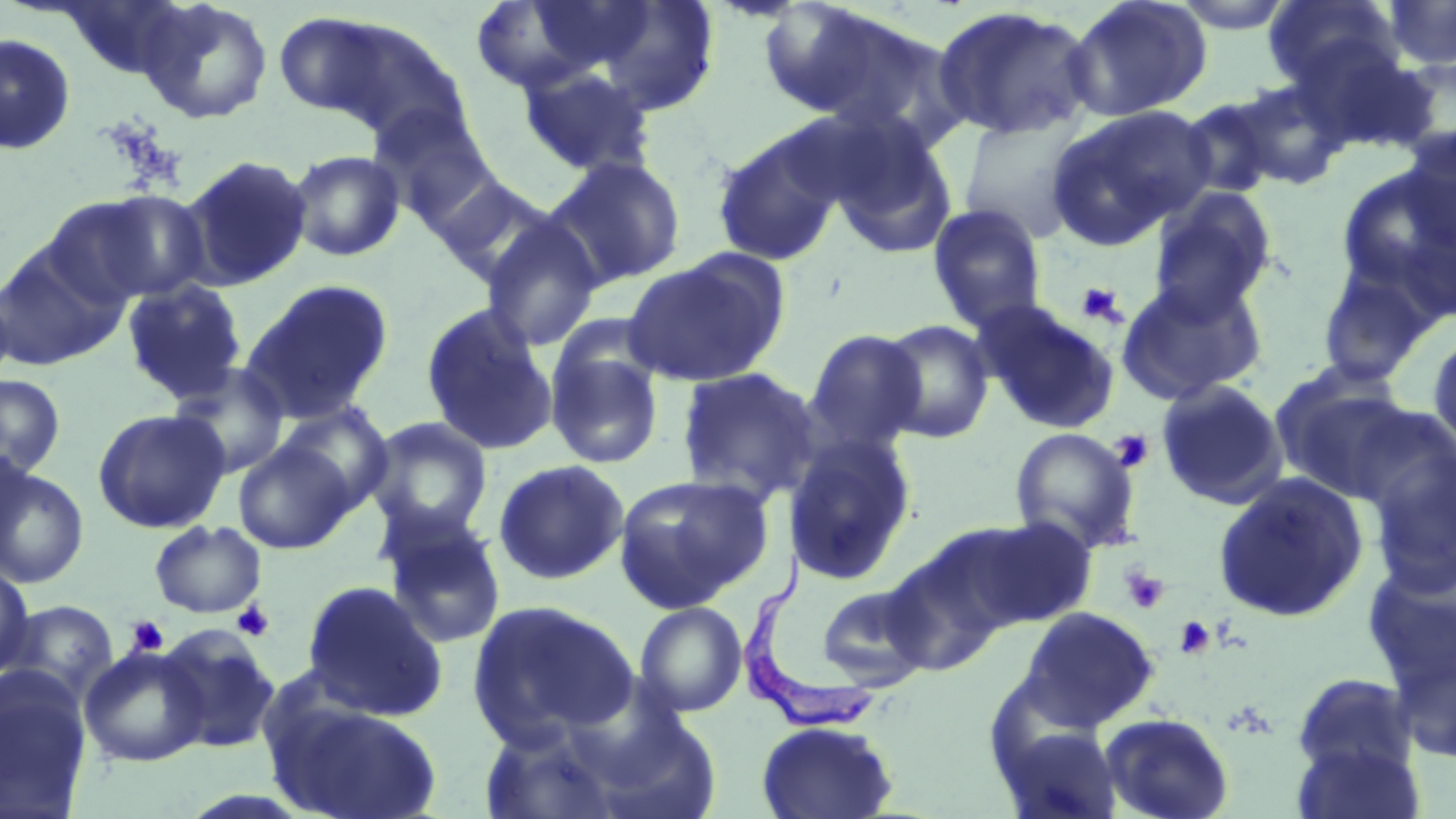
Summary:
  - Coordinate format: approximate bounding boxes as [x1, y1, x2, y2] in pixels
  - Platelet locations: [1075, 281, 1126, 326], [1109, 429, 1154, 473], [1121, 567, 1169, 614], [231, 601, 275, 642], [126, 616, 168, 656], [1174, 616, 1215, 660]
  - Trypanosoma brucei locations: [735, 550, 880, 731]
  - Uninfected red blood cell locations: [57, 0, 197, 79], [756, 0, 898, 121], [1063, 0, 1214, 122], [1170, 0, 1298, 34], [1262, 0, 1404, 92], [136, 1, 274, 124], [469, 1, 605, 95], [585, 1, 721, 117], [1383, 1, 1456, 71], [930, 5, 1099, 141], [787, 6, 961, 147], [273, 10, 397, 122], [319, 16, 470, 144], [0, 33, 76, 155], [1289, 36, 1440, 156], [1394, 56, 1456, 161], [518, 64, 657, 178], [1230, 79, 1350, 190], [1178, 94, 1286, 200], [368, 104, 495, 227], [1044, 104, 1213, 247], [958, 112, 1092, 243], [826, 119, 959, 260], [1399, 127, 1456, 251], [711, 129, 846, 266], [287, 149, 406, 262], [179, 154, 312, 291], [545, 156, 687, 288], [1335, 166, 1456, 311], [427, 173, 566, 287], [1147, 188, 1278, 319], [73, 189, 214, 303], [927, 204, 1048, 333], [479, 214, 604, 351], [0, 245, 125, 371], [622, 254, 786, 388], [1315, 261, 1440, 387], [1115, 275, 1270, 406], [121, 279, 247, 404], [241, 279, 394, 423], [974, 300, 1122, 435], [420, 303, 558, 457], [878, 319, 994, 443], [804, 328, 927, 453], [1427, 329, 1456, 453], [545, 339, 665, 470], [168, 362, 290, 479], [675, 367, 822, 504], [1270, 368, 1420, 503], [0, 373, 66, 480], [1154, 379, 1288, 509], [277, 402, 394, 512], [1346, 402, 1456, 528], [92, 408, 230, 533], [365, 417, 493, 538], [1009, 426, 1142, 555], [782, 433, 918, 587], [233, 440, 356, 554], [1364, 440, 1456, 597], [492, 459, 630, 585], [0, 465, 89, 589], [613, 473, 774, 612], [1213, 473, 1369, 623], [378, 509, 507, 650], [960, 515, 1098, 631], [149, 521, 267, 618], [881, 535, 1014, 678], [1362, 556, 1455, 701], [0, 566, 35, 678], [301, 578, 449, 721], [816, 584, 931, 690], [467, 599, 639, 746], [3, 600, 119, 703], [634, 601, 748, 717], [1020, 606, 1160, 731], [157, 625, 281, 754], [79, 646, 208, 767], [1291, 672, 1418, 779], [0, 675, 91, 818], [268, 700, 445, 818], [1099, 711, 1234, 819], [755, 720, 900, 819], [996, 722, 1123, 819], [479, 723, 626, 819], [1291, 739, 1425, 819]
  - Slide-level diagnosis: Trypanosoma brucei
  - Image size: 1456×819 pixels
  - Magnification: 1000x
  - Field of view: single
  - Modality: optical microscopy
  - Stain: May-Grünwald-Giemsa
  - Preparation: thin blood film